Classify this cell by malaria status.
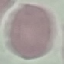

Uninfected.

Summary:
  - Stain: Giemsa
  - Image type: cell patch, automatically extracted from a larger field of view and resized to 64 × 64 pixels
  - Preparation: thin blood film
  - Capture: smartphone camera at the microscope eyepiece